Assess this cell for malaria.
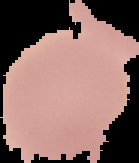

It is uninfected.

Cell region segmented out of the field of view; the surrounding area is masked to black. From a thin blood film. Image is 139×163 pixels.